Classify this cell by malaria status.
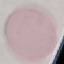

It is uninfected.

{
  "stain": "Giemsa",
  "capture": "smartphone through the microscope eyepiece",
  "image_type": "cell patch, automatically extracted from a larger field of view and resized to 64 × 64 pixels",
  "preparation": "thin smear"
}